Report the malaria status of this cell.
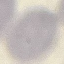
Uninfected.

Acquired by smartphone through the microscope eyepiece. Cell patch, automatically extracted from a larger field of view and resized to 64 × 64 pixels. Giemsa-stained preparation. Thin blood smear.